Report the malaria status of this cell.
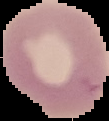

Uninfected.

Segmented cell region on a black background. From a thin blood film. Image is 109×121 pixels.